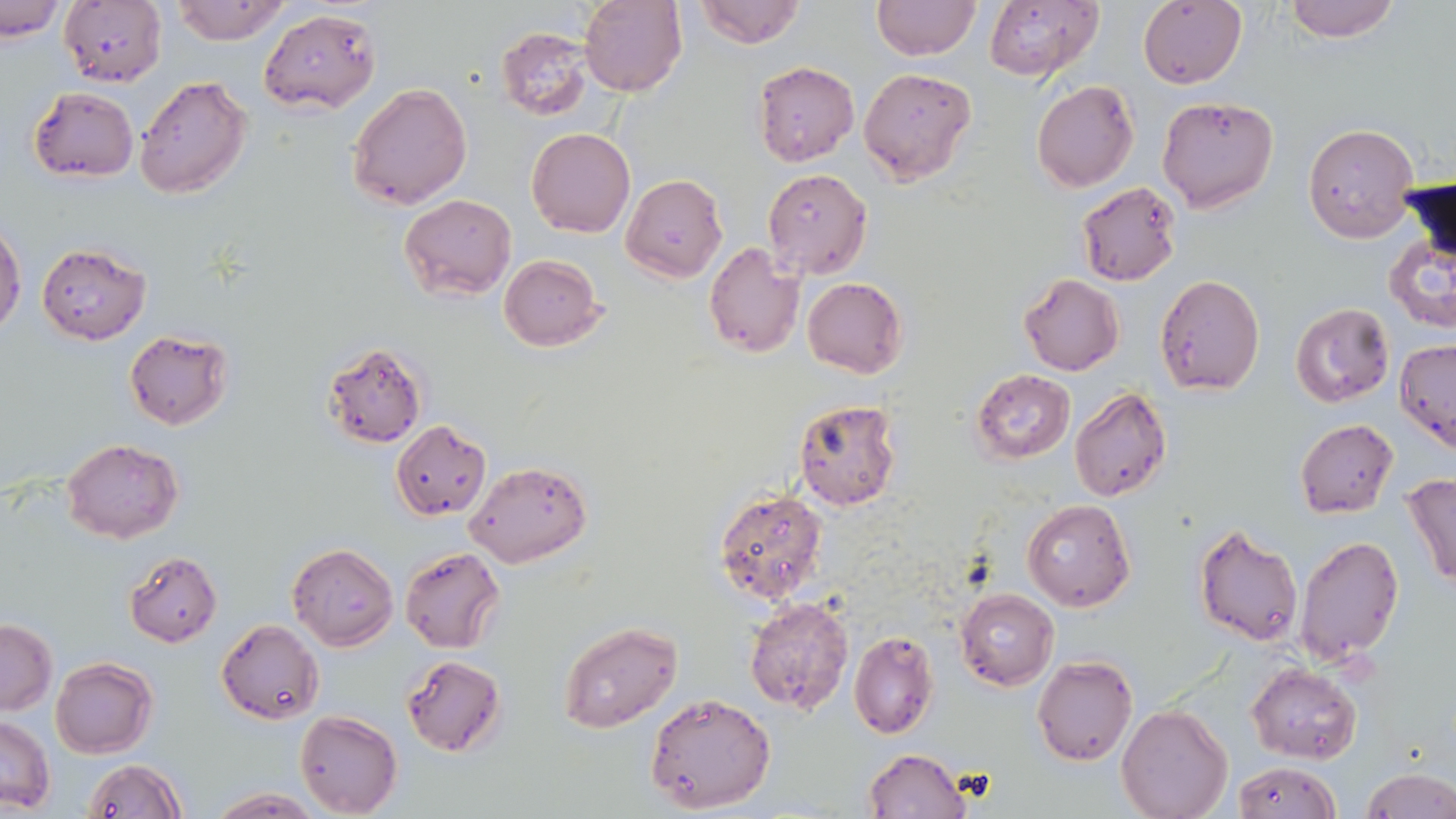
Approximate bounding boxes as (x1, y1, x2, y2) in pixels. Uninfected red blood cell locations: (60, 0, 168, 87), (168, 0, 294, 46), (579, 0, 687, 96), (693, 0, 804, 49), (872, 0, 980, 60), (1138, 0, 1248, 89), (1280, 0, 1402, 42), (1, 1, 66, 41), (983, 1, 1104, 82), (258, 7, 381, 114), (496, 26, 594, 120), (753, 61, 859, 166), (858, 67, 977, 185), (133, 74, 253, 199), (1031, 80, 1139, 192), (347, 82, 472, 211), (27, 86, 138, 182), (1156, 96, 1278, 212), (1302, 124, 1418, 243), (527, 128, 635, 238), (762, 169, 873, 279), (621, 173, 727, 282), (1076, 180, 1183, 286), (400, 194, 516, 301), (0, 224, 26, 337), (1384, 224, 1456, 336), (704, 241, 804, 359), (37, 244, 151, 345), (498, 255, 605, 351), (1155, 273, 1266, 394), (1019, 274, 1124, 376), (802, 277, 909, 379), (1291, 301, 1395, 409), (124, 329, 234, 430), (1395, 338, 1456, 453), (322, 341, 427, 449), (971, 368, 1075, 464), (1068, 386, 1171, 502), (791, 399, 903, 509), (1295, 418, 1398, 518), (391, 420, 492, 520), (62, 437, 183, 544), (465, 461, 592, 568), (1403, 473, 1456, 588), (714, 488, 830, 607), (1022, 499, 1137, 612), (1193, 523, 1304, 647), (1294, 533, 1405, 668), (286, 541, 398, 651), (399, 547, 505, 654), (124, 550, 223, 646), (955, 588, 1058, 691), (743, 595, 853, 716), (0, 619, 58, 715), (217, 619, 323, 725), (556, 620, 684, 734), (848, 631, 938, 739), (400, 654, 506, 757), (1032, 655, 1138, 765), (50, 657, 158, 757), (1245, 662, 1362, 765), (645, 691, 776, 813), (1117, 702, 1232, 818), (295, 711, 403, 818), (0, 714, 57, 814), (864, 748, 971, 818), (82, 757, 185, 818), (1229, 760, 1342, 819), (1361, 769, 1456, 819), (205, 787, 324, 817). Slide-level diagnosis: Plasmodium falciparum. Thin blood smear. 1000x magnification. Optical microscopy. May-Grünwald-Giemsa stain. Image is 1456×819 pixels. One field of a larger specimen.